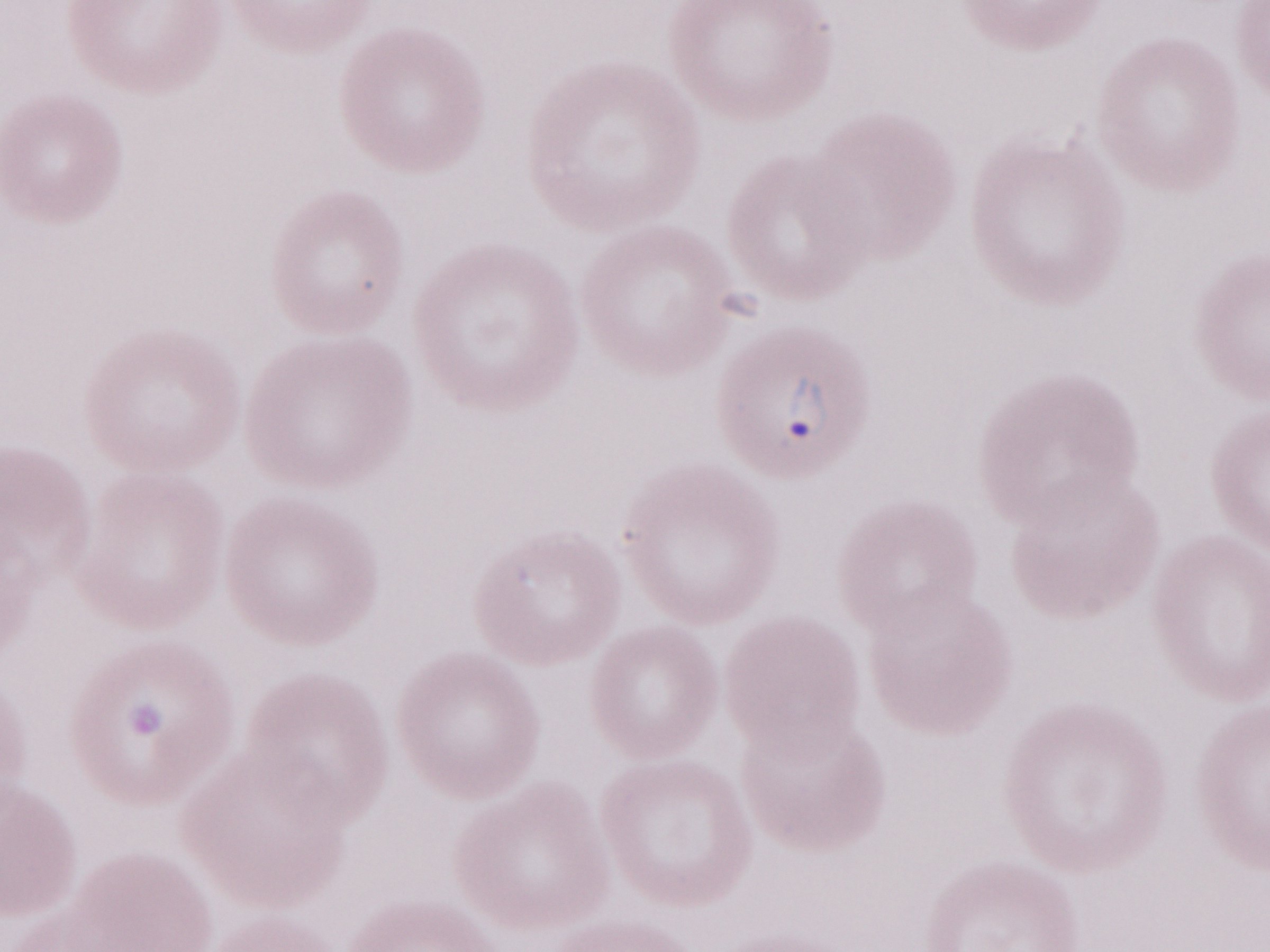

Magnification: 1,000x. Olympus BX43 microscope and DP73 digital camera. Thin peripheral-blood smear. May-Grünwald-Giemsa (MGG) stain. Single field of view. Image is 1270×952 pixels. Patient diagnosis: malaria infection.